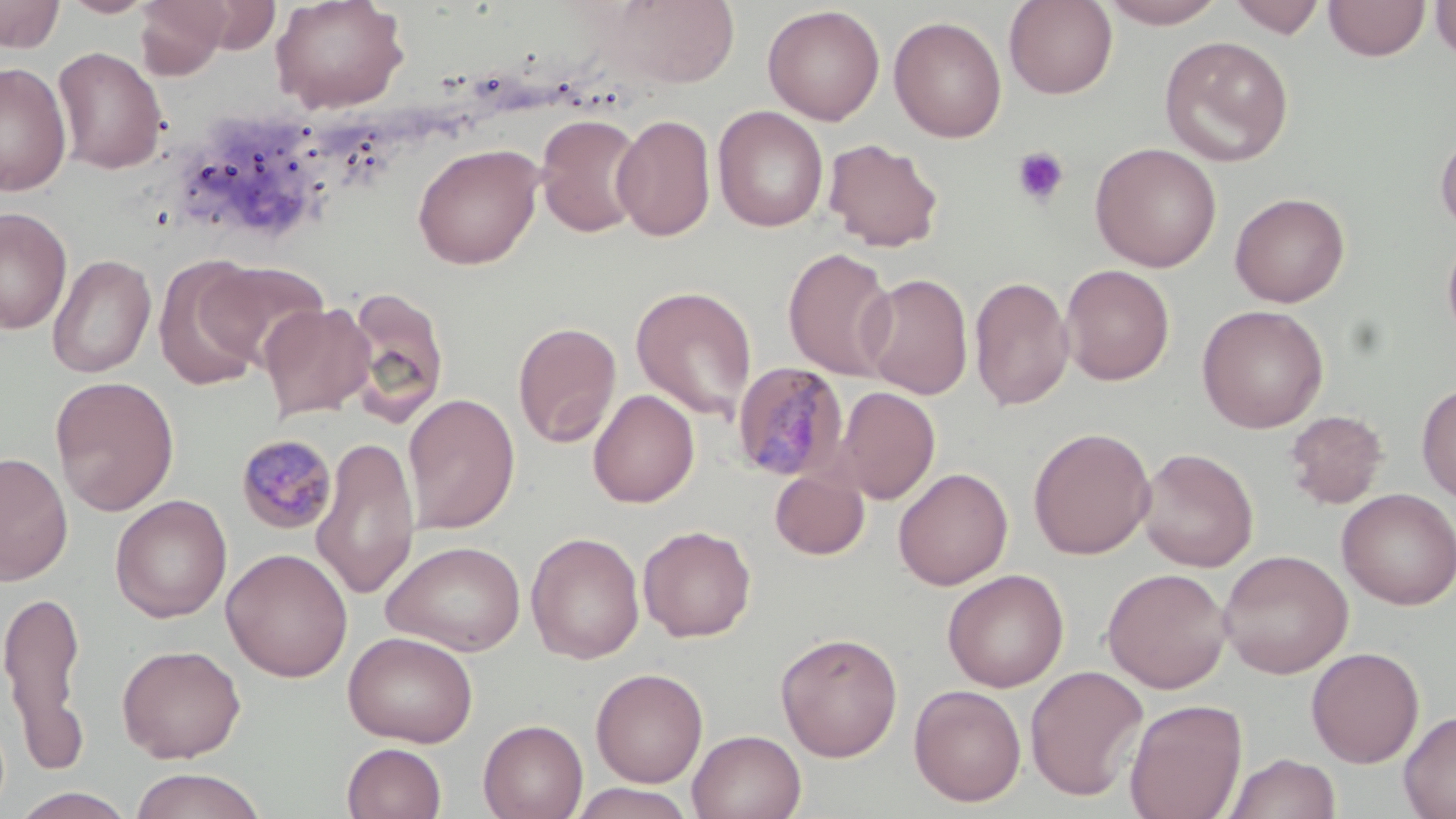
Approximate bounding boxes as (x1,y1)-(x2,y2) corner pairs in pixels. Plasmodium malariae-infected red blood cell locations: (731,361)-(850,481), (235,433)-(338,534). Platelet locations: (1011,146)-(1070,207). Uninfected red blood cell locations: (0,0)-(65,53), (60,0)-(157,18), (135,0)-(231,78), (269,0)-(410,114), (1003,0)-(1118,99), (1099,0)-(1228,28), (1228,0)-(1326,38), (1325,0)-(1430,61), (1431,0)-(1456,63), (611,1)-(740,87), (762,5)-(885,125), (889,15)-(1007,143), (1160,35)-(1294,167), (52,46)-(168,174), (0,62)-(72,196), (713,106)-(829,232), (612,113)-(716,242), (535,114)-(648,239), (1435,129)-(1456,237), (823,137)-(945,252), (1090,142)-(1222,272), (412,143)-(544,269), (1229,191)-(1350,307), (0,206)-(73,334), (1441,229)-(1456,347), (783,247)-(897,380), (47,253)-(157,379), (154,256)-(268,392), (200,259)-(329,369), (1060,264)-(1175,385), (860,273)-(974,399), (969,275)-(1074,411), (342,285)-(451,429), (630,285)-(758,422), (259,301)-(375,421), (1196,304)-(1329,433), (513,320)-(622,448), (50,375)-(179,516), (1416,381)-(1456,503), (834,386)-(941,504), (588,389)-(699,508), (403,393)-(520,534), (1284,410)-(1388,509), (1028,426)-(1156,560), (312,435)-(420,600), (1136,447)-(1259,572), (0,451)-(73,586), (769,466)-(870,560), (893,467)-(1013,590), (1336,488)-(1456,609), (110,494)-(232,623), (638,524)-(757,642), (526,531)-(645,664), (382,539)-(526,656), (220,547)-(354,682), (1217,549)-(1354,679), (1102,567)-(1232,694), (942,569)-(1069,692), (0,584)-(89,769), (344,630)-(478,746), (774,631)-(903,762), (117,643)-(245,762), (1306,646)-(1424,767), (1025,665)-(1149,802), (591,667)-(708,787), (909,683)-(1027,807), (1124,698)-(1248,818), (1398,710)-(1456,819), (478,719)-(587,819), (687,729)-(807,819), (342,742)-(447,819), (1225,752)-(1341,819), (128,768)-(268,819), (568,783)-(695,819), (10,787)-(137,819). Slide-level diagnosis: Plasmodium malariae. One field of a larger specimen. Image is 1456×819 pixels. May-Grünwald-Giemsa-stained preparation. Optical microscopy. Thin blood film. Captured at 1000x magnification.